Classify this cell by malaria status.
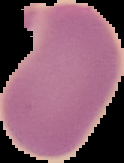
Uninfected.

image size = 124×163 pixels
image type = cell region segmented out of the field of view; surrounding area masked to black
preparation = thin blood film